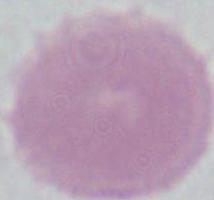

A red blood cell is shown. Photomicrograph. Captured at 1000x magnification.